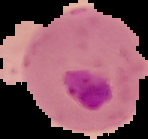

Summary:
  - Result: Plasmodium parasites identified
  - Image size: 148×139 pixels
  - Image type: segmented cell region on a black background
  - Preparation: thin blood smear